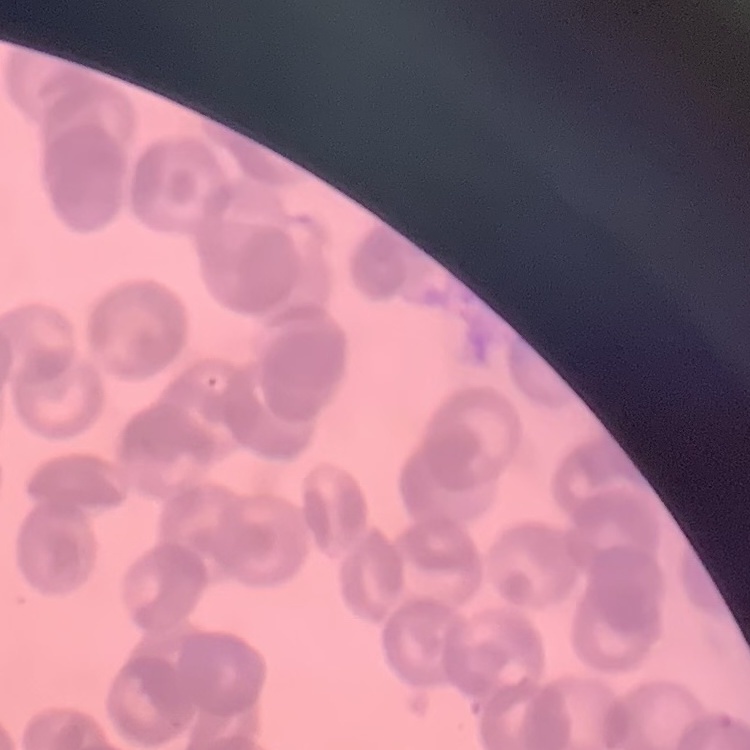

Summary:
  - Erythrocyte morphology: rouleaux formation
  - Stain: Field's or Giemsa
  - Image type: square crop of a larger photomicrograph
  - Preparation: thin blood film